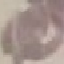

malaria_status: uninfected
image_type: cell patch, automatically extracted from a larger field of view and resized to 64 × 64 pixels
capture: smartphone camera at the microscope eyepiece
preparation: thin blood smear
stain: Giemsa